Locate every malaria parasite and every leukocyte.
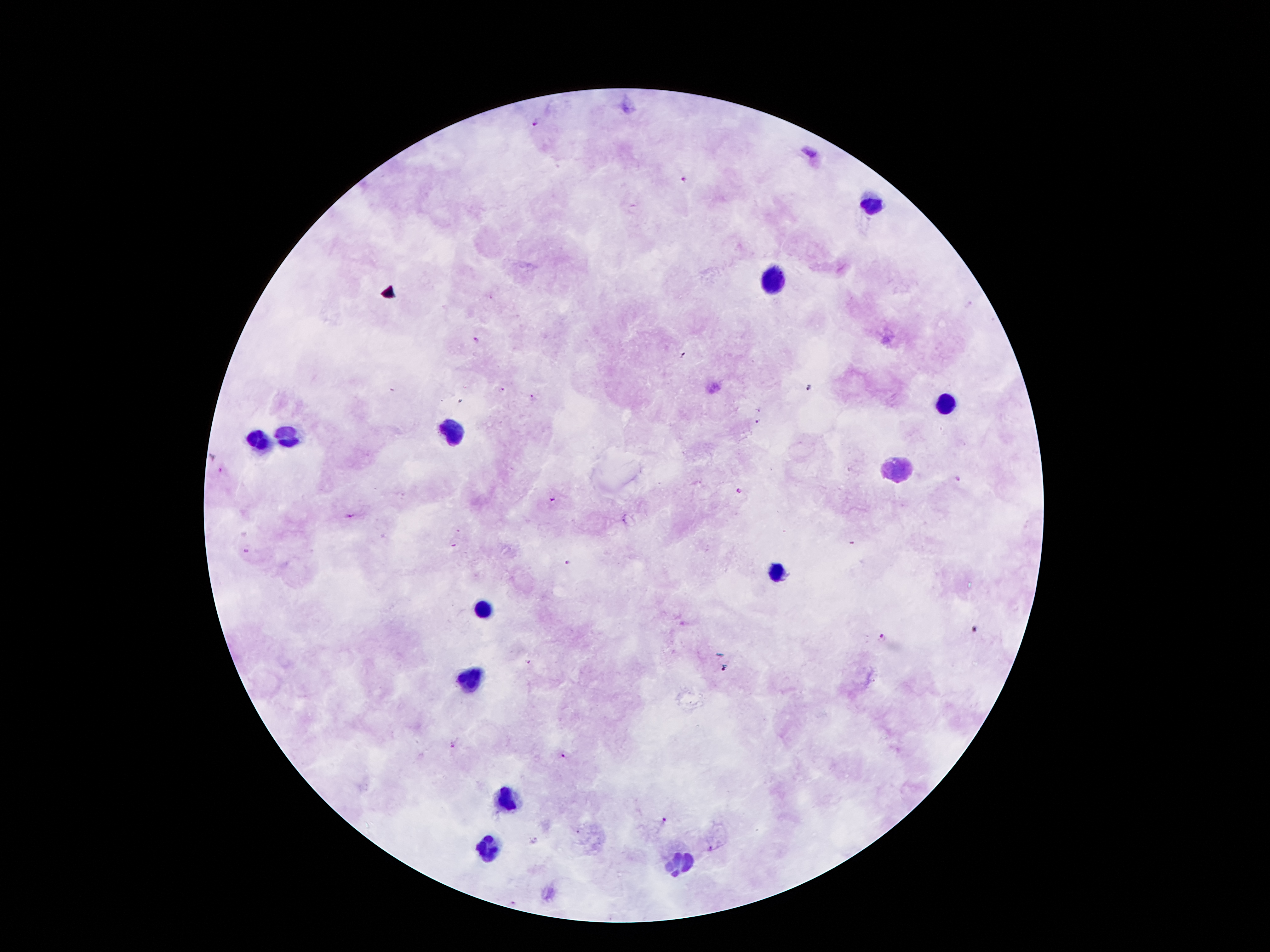

Approximate centers as (x, y) in pixels.
Malaria parasites: (533, 123), (682, 180), (475, 339), (810, 388), (503, 390), (532, 398), (757, 421), (222, 470), (959, 479), (740, 490), (551, 498), (351, 517), (246, 552), (567, 562), (882, 637), (528, 662), (723, 670), (453, 746), (563, 757), (665, 820), (711, 850), (515, 903).
Leukocytes: (872, 204), (773, 277), (948, 405), (286, 435), (452, 435), (263, 440), (895, 470), (776, 573), (482, 608), (470, 680), (503, 800), (489, 847), (682, 865).

Summary:
  - Magnification: 100x
  - Capture: smartphone camera through the microscope eyepiece
  - Preparation: thick blood smear
  - Field of view: single
  - Image size: 1270×952 pixels
  - Patient malaria status: infected with Plasmodium falciparum
  - Stain: Giemsa